Assess this cell for malaria.
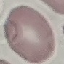

Uninfected.

Summary:
  - Image type: cell patch, automatically extracted from a larger field of view and resized to 64 × 64 pixels
  - Capture: smartphone camera at the microscope eyepiece
  - Preparation: thin smear
  - Stain: Giemsa